Identify the parasite.
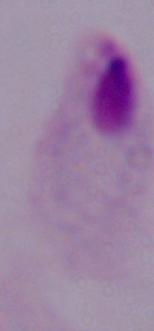

A trichomonad.

modality: micrograph
magnification: 1000x